Point out each leukocyte.
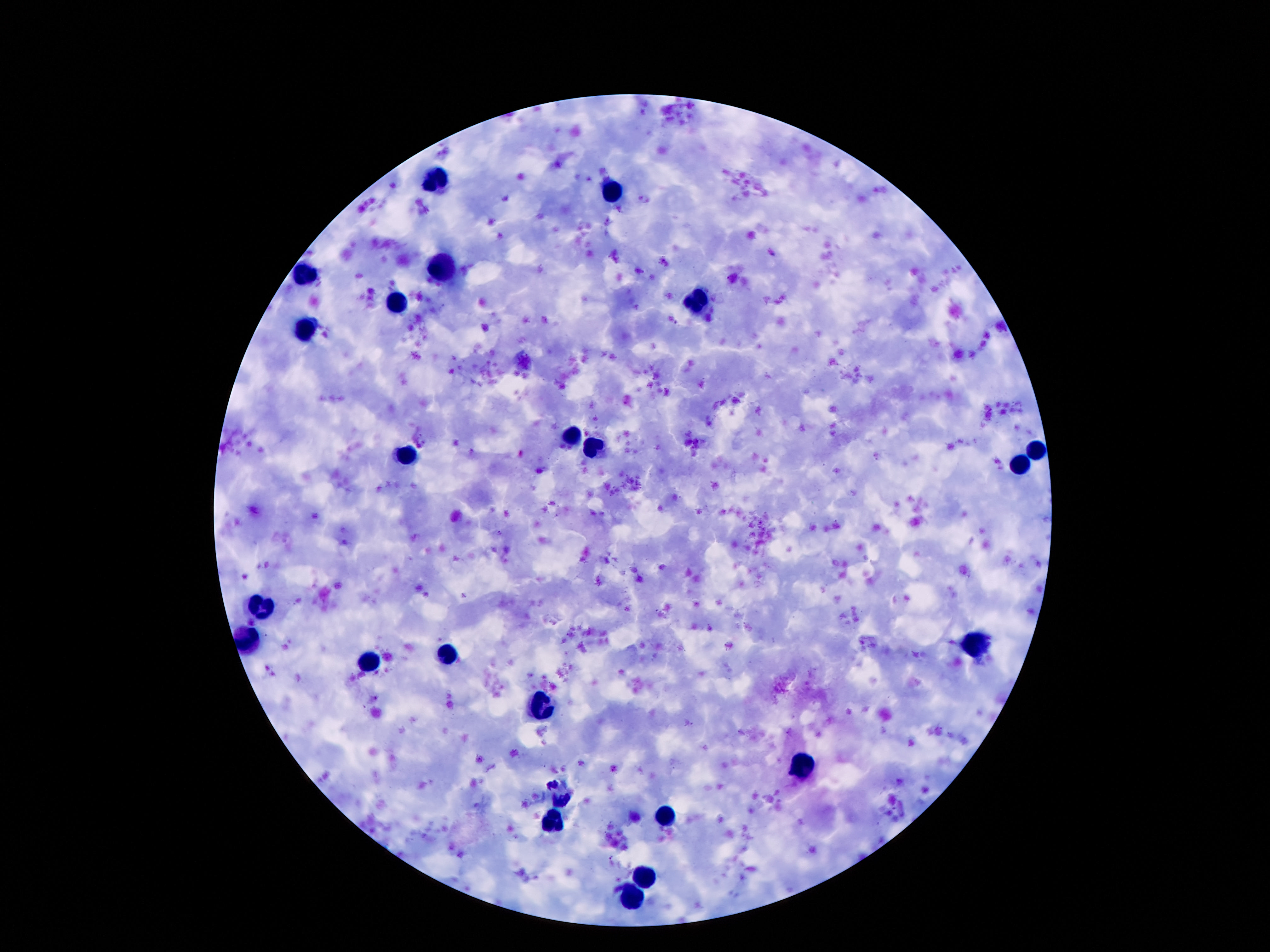
Approximate centers as {x, y} in pixels.
Leukocytes: {437, 175}, {614, 190}, {442, 268}, {303, 273}, {701, 302}, {398, 306}, {307, 329}, {571, 434}, {595, 444}, {1034, 451}, {410, 453}, {1018, 467}, {262, 605}, {249, 640}, {970, 643}, {449, 654}, {370, 661}, {540, 704}, {801, 762}, {667, 816}, {554, 822}, {645, 874}, {634, 899}.

100x magnification. One field from this slide. Giemsa-stained preparation. Thick blood smear. Patient malaria status: negative. Image is 1270×952 pixels. Photographed through the microscope eyepiece with a smartphone camera.